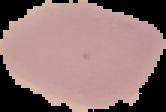
Summary:
  - Image size: 166×112 pixels
  - Result: negative for Plasmodium parasites
  - Preparation: thin blood smear
  - Image type: segmented cell region on a black background